Assess the morphology of the red blood cells.
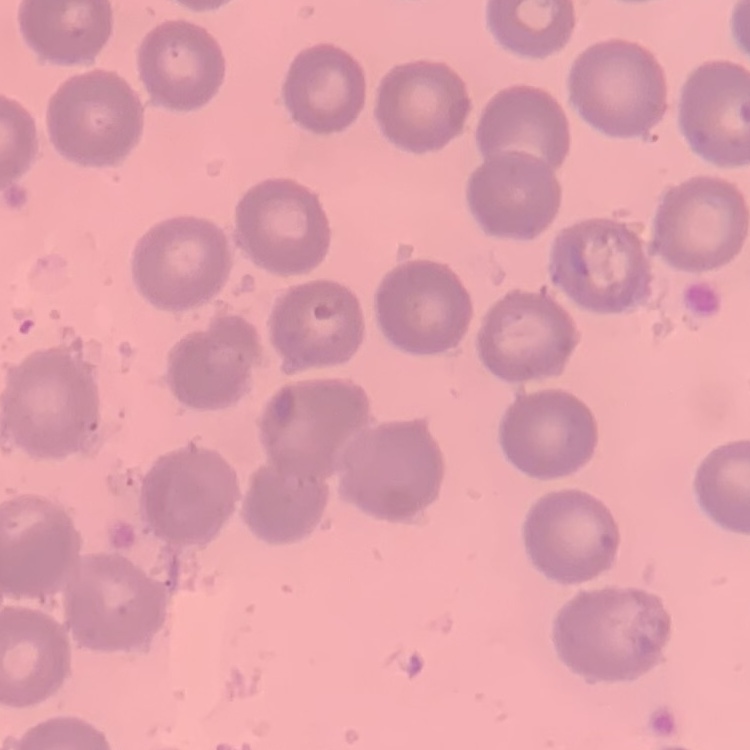

No rouleaux formation.

Thin blood film. Square crop of a larger photomicrograph. Stained with either Field's or Giemsa.